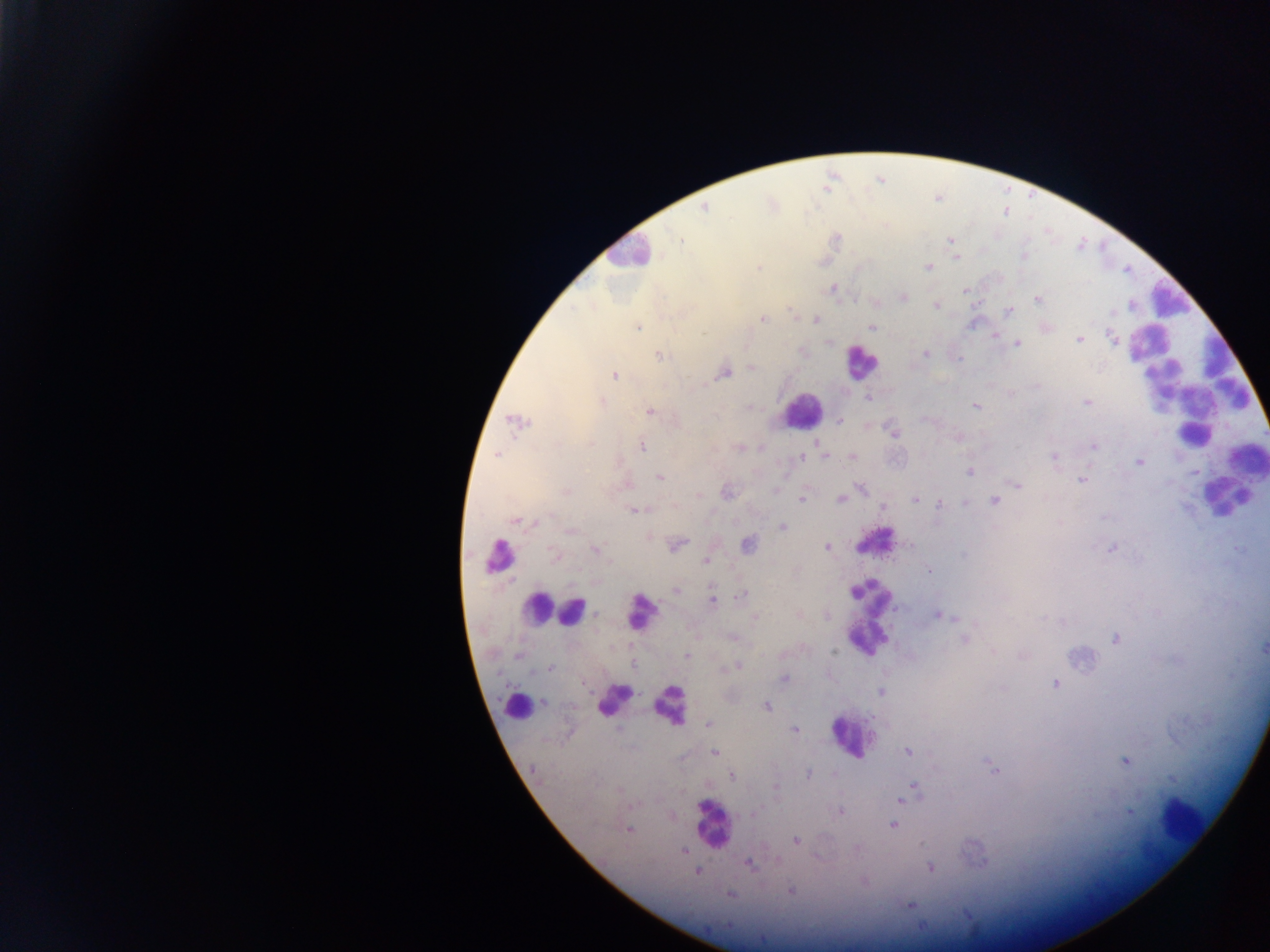

Approximate centers as (x, y) in pixels. Leukocyte locations: (626, 251), (1169, 301), (860, 362), (1195, 386), (800, 409), (1219, 491), (873, 541), (498, 556), (535, 606), (870, 609), (577, 612), (638, 612), (609, 697), (514, 703), (669, 703), (851, 737), (1175, 819), (711, 821). Malaria parasite locations: (704, 208), (680, 239), (950, 240), (1024, 255), (956, 257), (928, 267), (759, 268), (833, 289), (964, 290), (903, 297), (1037, 299), (936, 306), (1008, 311), (762, 319), (816, 320), (637, 327), (872, 327), (1046, 328), (996, 336), (1112, 338), (1079, 340), (829, 343), (1018, 343), (802, 352), (925, 354), (660, 355), (752, 368), (724, 373), (614, 375), (868, 397), (602, 402), (1086, 402), (976, 406), (649, 412), (841, 420), (515, 421), (892, 431), (590, 444), (1093, 446), (641, 447), (497, 454), (824, 455), (801, 456), (852, 458), (1054, 458), (1140, 462), (970, 472), (659, 477), (1082, 480), (1017, 484), (861, 488), (566, 491), (774, 491), (727, 492), (699, 495), (801, 499), (840, 500), (915, 500), (994, 501), (939, 503), (965, 503), (883, 508), (634, 510), (516, 522), (783, 527), (571, 531), (649, 537), (677, 544), (911, 545), (746, 546), (827, 547), (1112, 549), (595, 550), (555, 555), (963, 555), (706, 561), (929, 571), (676, 589), (741, 595), (712, 601), (827, 616), (938, 616), (756, 618), (733, 637), (964, 639), (1114, 639), (1263, 647), (834, 651), (993, 651), (686, 655), (517, 656), (633, 666), (737, 666), (550, 668), (730, 668), (783, 679), (1054, 684), (881, 692), (544, 702), (766, 706), (708, 724), (795, 730), (909, 751), (714, 752), (1124, 762), (992, 767), (809, 775), (732, 776), (776, 786), (914, 787), (902, 800), (840, 811), (1130, 812), (754, 813), (892, 826), (629, 830), (796, 841), (857, 848), (684, 851), (777, 861), (749, 865), (930, 867), (697, 872), (791, 891), (731, 895), (909, 906). One field of view. Mobile-phone photograph taken through the microscope. Image is 1270×952 pixels. Thick blood smear. Collected in Ghana.